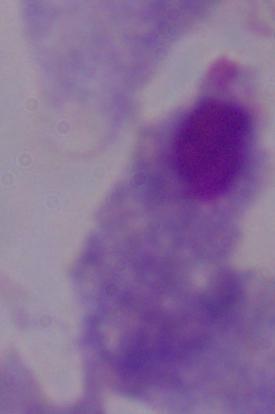

identification = trichomonad
modality = micrograph
magnification = 1000x